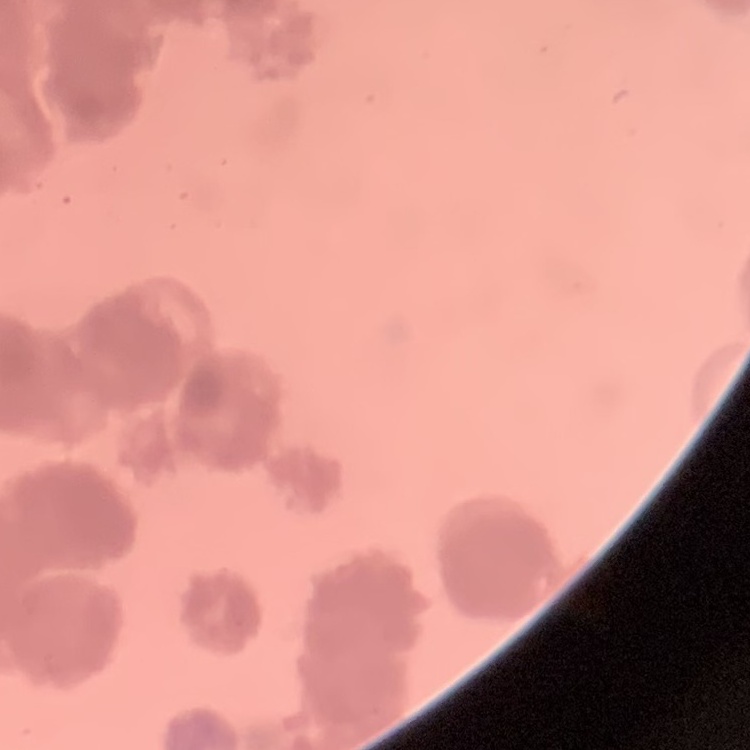

The erythrocytes show rouleaux formation. Thin blood smear. Square crop of a larger photomicrograph. Field's or Giemsa stain.